Assess this cell for malaria.
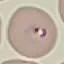
Parasitized.

Summary:
  - Image type: automatically extracted cell patch, resized to 64 × 64 pixels
  - Preparation: thin smear
  - Stain: Giemsa
  - Capture: smartphone camera at the microscope eyepiece